Locate every uninfected red blood cell.
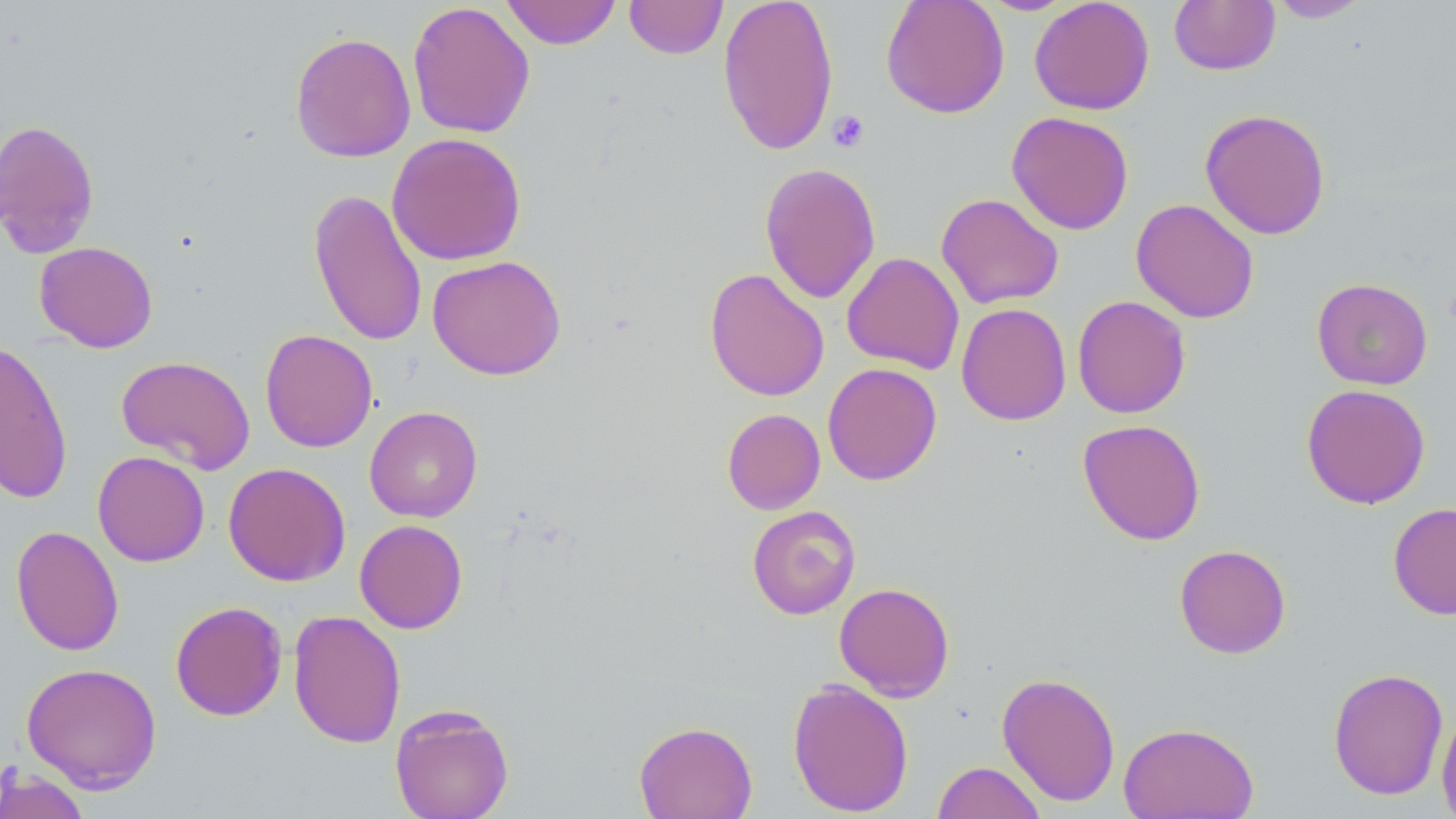
Approximate bounding boxes as [x1, y1, x2, y2] in pixels.
Uninfected red blood cells: [501, 0, 621, 49], [624, 0, 728, 59], [717, 0, 839, 156], [880, 0, 1009, 118], [976, 0, 1077, 15], [1029, 0, 1154, 115], [1169, 0, 1280, 76], [1266, 0, 1373, 23], [407, 1, 535, 139], [290, 31, 416, 163], [1199, 108, 1331, 240], [1006, 111, 1134, 235], [1, 118, 100, 258], [386, 132, 527, 266], [759, 162, 881, 304], [308, 188, 427, 347], [936, 192, 1064, 309], [1131, 198, 1259, 324], [34, 241, 158, 352], [842, 252, 964, 374], [427, 254, 566, 380], [704, 267, 830, 402], [1311, 277, 1433, 390], [1072, 295, 1191, 419], [956, 303, 1071, 426], [259, 329, 378, 453], [0, 339, 73, 504], [116, 355, 255, 474], [822, 362, 942, 486], [1301, 383, 1431, 509], [364, 406, 483, 522], [722, 408, 825, 514], [1077, 419, 1206, 545], [92, 450, 210, 567], [223, 462, 350, 586], [1388, 502, 1456, 620], [746, 505, 861, 620], [354, 519, 468, 634], [10, 525, 124, 657], [1174, 544, 1292, 659], [834, 582, 955, 702], [169, 601, 287, 721], [288, 609, 406, 749], [20, 661, 163, 792], [1327, 667, 1449, 800], [997, 671, 1121, 806], [787, 678, 914, 816], [389, 703, 514, 819], [1436, 707, 1456, 818], [634, 720, 758, 819], [1117, 721, 1259, 818], [931, 760, 1047, 819], [0, 766, 93, 819].

{
  "slide_level_diagnosis": "negative for blood parasites",
  "field_of_view": "one of a larger specimen",
  "stain": "May-Grünwald-Giemsa",
  "magnification": "1000x",
  "image_size": "1456×819 pixels",
  "preparation": "thin blood film",
  "modality": "light microscopy",
  "platelet_locations": "approximate bounding boxes as [x1, y1, x2, y2] in pixels: [827, 110, 870, 153]"
}